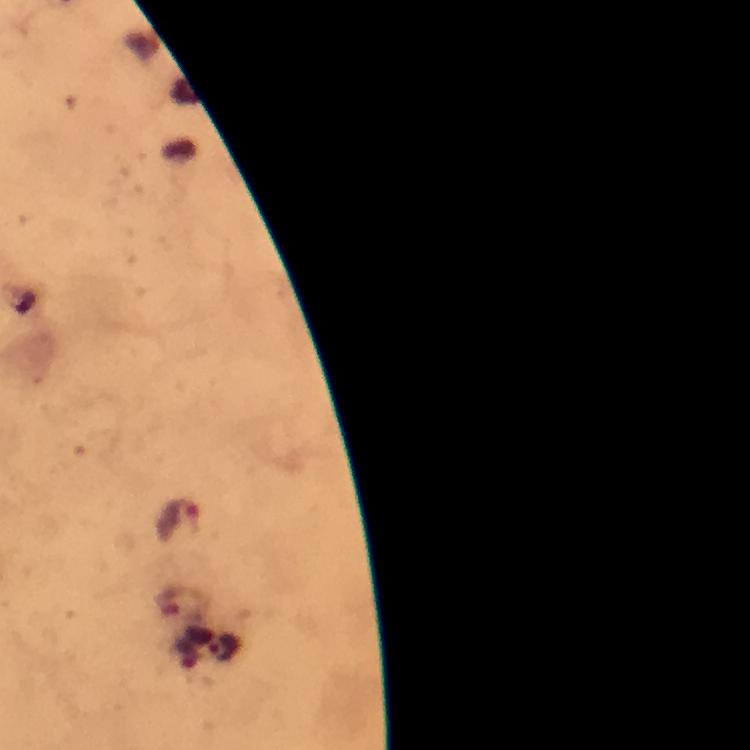

preparation = thick blood film
context = from a malaria diagnostic workup
immersion oil = used
capture = smartphone photograph through a microscope
malaria parasite locations = approximate object centers, in pixels from the top-left corner: (x=177, y=520)
magnification = 100x
image size = 750×750 pixels
cropped from = one field of view
stain = Giemsa